Point out every malaria parasite.
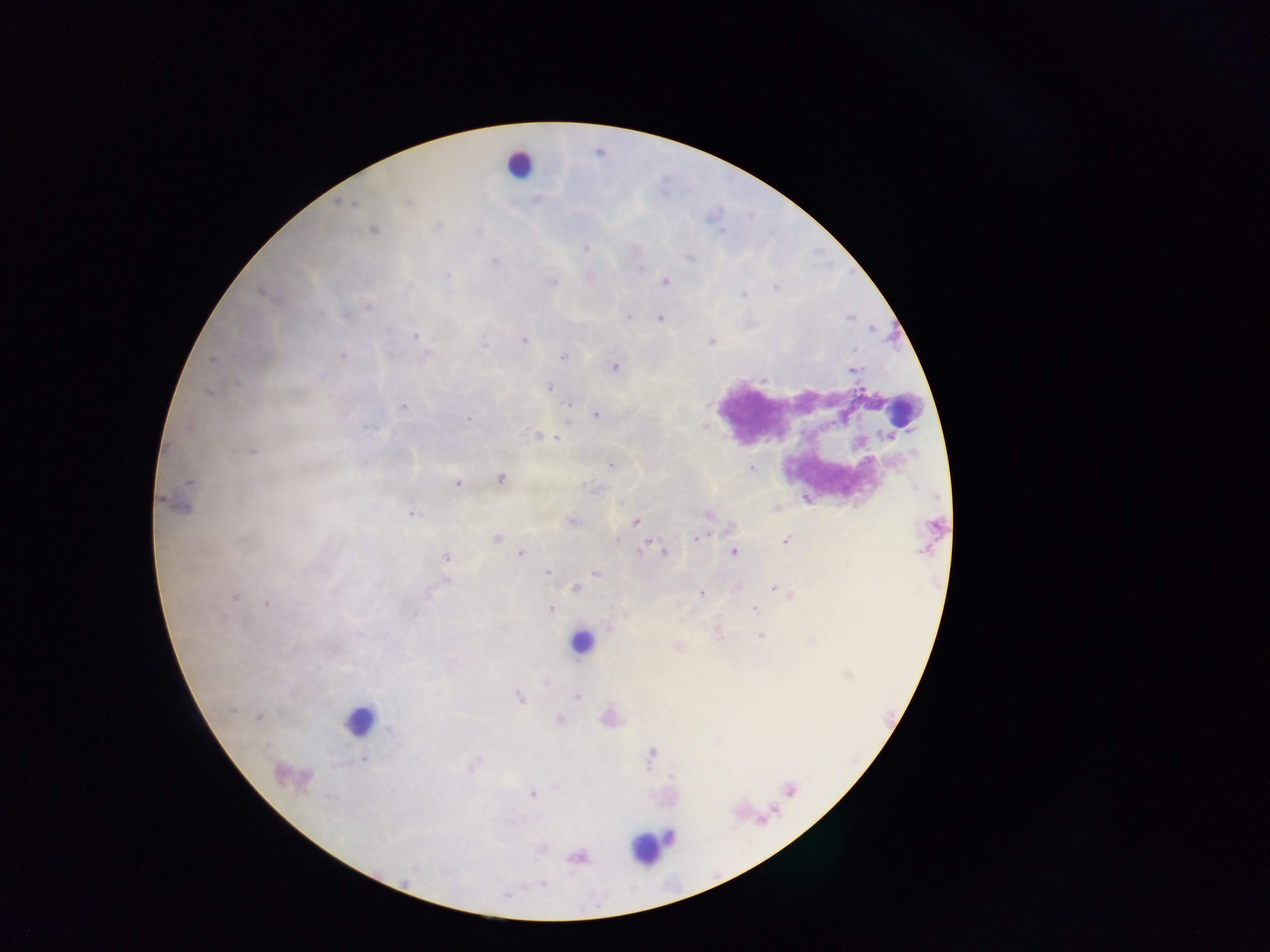

Approximate centers as x y in pixels.
Malaria parasites: 408 203; 439 226; 372 229; 585 249; 689 257; 493 261; 664 280; 551 281; 262 292; 367 306; 627 316; 661 317; 416 336; 524 341; 710 341; 485 344; 425 354; 342 355; 564 355; 211 360; 614 366; 853 370; 550 387; 209 392; 569 404; 402 406; 595 414; 468 419; 567 421; 189 427; 535 435; 557 438; 252 451; 611 464; 752 468; 501 478; 457 483; 180 501; 774 508; 411 512; 708 514; 571 521; 635 521; 695 538; 495 539; 785 541; 643 547; 733 551; 663 552; 520 553; 446 556; 547 571; 594 573; 447 582; 575 588; 772 588; 778 590; 701 593; 790 594; 232 597; 268 602; 754 608; 551 609; 413 614; 609 629; 718 630; 677 646; 451 662; 545 680; 577 695; 519 698; 257 717; 608 718; 558 719; 473 765; 287 774; 532 794; 540 849; 576 858; 542 884.

field of view = single
capture = mobile-phone photograph through a microscope
image size = 1270×952 pixels
leukocyte locations = approximate centers as x y in pixels: 518 164; 903 409; 582 641; 360 722; 789 790; 663 839; 649 845
preparation = thick blood smear
country = Ghana